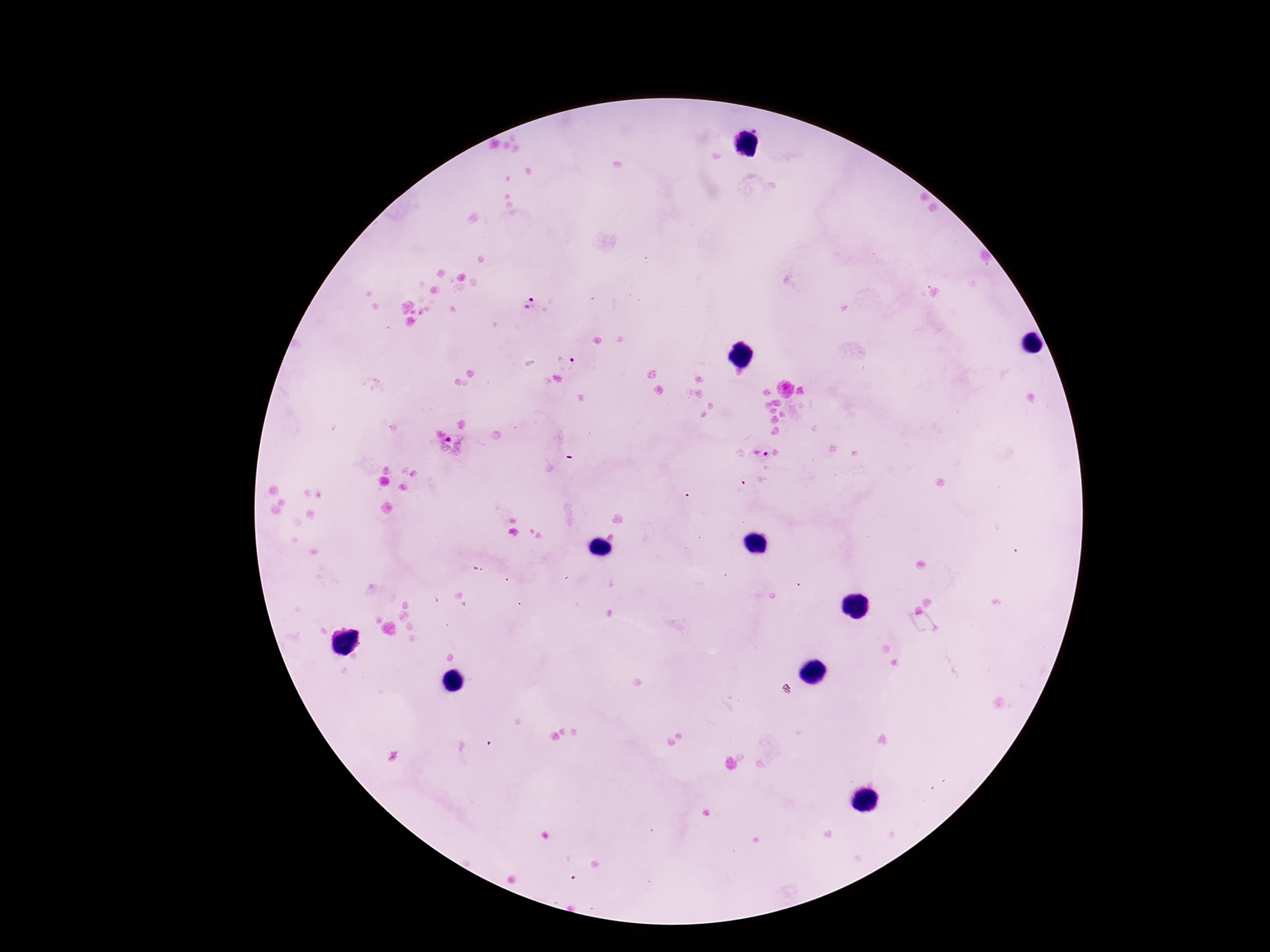
capture = smartphone camera through the microscope eyepiece
field of view = one from this slide
preparation = thick peripheral-blood smear
Plasmodium parasite locations = approximate centers as {x, y} in pixels: {530, 304}, {566, 362}, {454, 445}, {762, 452}
stain = Giemsa
magnification = 100x
patient malaria status = infected
image size = 1270×952 pixels